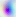

Micrograph. Captured at 400x magnification. Toxoplasma gondii is shown.